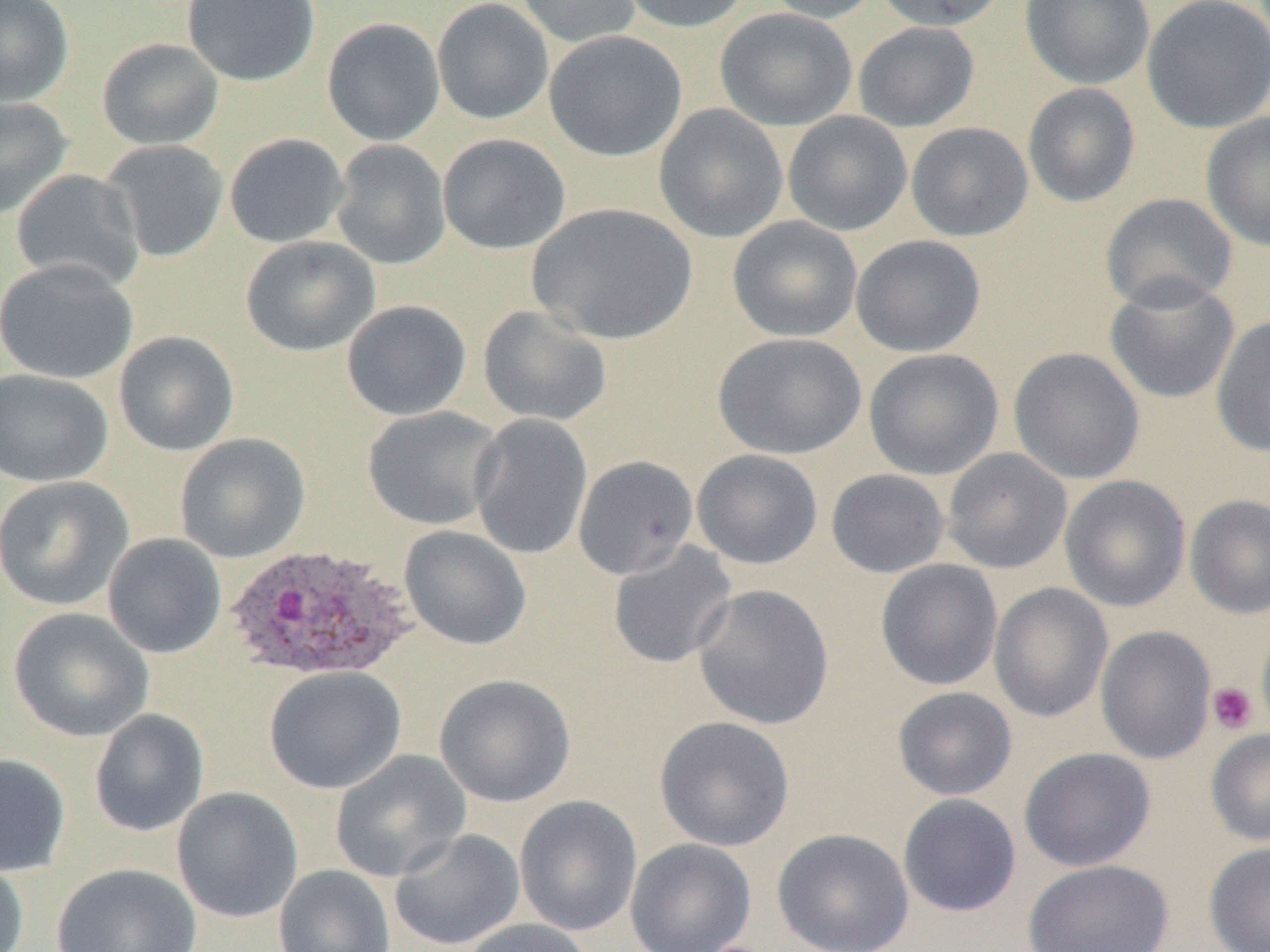
{
  "slide_level_diagnosis": "Plasmodium ovale",
  "modality": "light microscopy",
  "platelet_locations": "approximate bounding boxes as [x1, y1, x2, y2] in pixels: [1207, 681, 1258, 734]",
  "magnification": "1000x",
  "image_size": "1270×952 pixels",
  "plasmodium_ovale_infected_red_blood_cell_locations": "approximate bounding boxes as [x1, y1, x2, y2] in pixels: [225, 543, 418, 682]",
  "field_of_view": "single",
  "uninfected_red_blood_cell_locations": "approximate bounding boxes as [x1, y1, x2, y2] in pixels: [0, 0, 75, 106], [182, 0, 320, 86], [432, 0, 554, 125], [515, 0, 642, 48], [616, 0, 755, 34], [760, 0, 883, 24], [874, 0, 1009, 31], [1020, 0, 1155, 89], [1141, 0, 1270, 134], [715, 8, 858, 131], [321, 17, 445, 146], [853, 21, 980, 132], [544, 30, 687, 162], [96, 37, 225, 150], [1023, 82, 1141, 208], [0, 97, 74, 219], [653, 103, 788, 243], [782, 111, 913, 237], [1201, 111, 1270, 251], [906, 122, 1033, 241], [224, 132, 349, 249], [438, 133, 571, 254], [330, 139, 451, 270], [100, 140, 229, 263], [10, 168, 145, 291], [1100, 193, 1237, 312], [527, 202, 697, 346], [727, 216, 863, 342], [240, 235, 380, 356], [851, 235, 986, 357], [0, 258, 138, 384], [1104, 277, 1240, 404], [342, 300, 472, 421], [478, 305, 612, 426], [1211, 315, 1270, 457], [113, 331, 240, 456], [713, 332, 867, 460], [1008, 347, 1145, 484], [863, 348, 1004, 480], [0, 369, 114, 488], [362, 406, 505, 530], [468, 414, 593, 560], [175, 433, 311, 563], [942, 448, 1072, 573], [692, 449, 823, 570], [573, 455, 699, 579], [826, 468, 950, 578], [1060, 475, 1191, 612], [0, 476, 134, 611], [1185, 495, 1270, 619], [399, 526, 532, 651], [102, 533, 227, 659], [608, 542, 737, 669], [876, 559, 1004, 690], [989, 582, 1113, 723], [693, 584, 834, 730], [8, 607, 154, 743], [1256, 614, 1270, 738], [1095, 625, 1216, 764], [263, 666, 407, 794], [434, 674, 576, 807], [893, 686, 1017, 801], [88, 708, 210, 838], [655, 716, 795, 851], [1206, 728, 1270, 846], [1018, 747, 1156, 872], [330, 750, 471, 882], [0, 752, 71, 876], [171, 787, 303, 923], [898, 794, 1022, 918], [514, 795, 642, 937], [388, 828, 526, 951], [773, 828, 914, 952], [625, 838, 757, 952], [1204, 842, 1270, 952], [0, 854, 30, 952], [1023, 859, 1173, 952], [51, 862, 203, 952], [273, 864, 396, 952], [459, 918, 597, 952]",
  "preparation": "thin blood smear"
}